Classify this cell by malaria status.
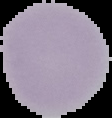
It is uninfected.

The area outside the segmented cell region is set to black. From a thin blood smear. Image is 112×118 pixels.